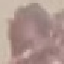
result = no malaria parasites seen
capture = smartphone camera at the microscope eyepiece
image type = automatically extracted cell patch, resized to 64 × 64 pixels
preparation = thin blood smear
stain = Giemsa